Locate every leukocyte (white blood cell).
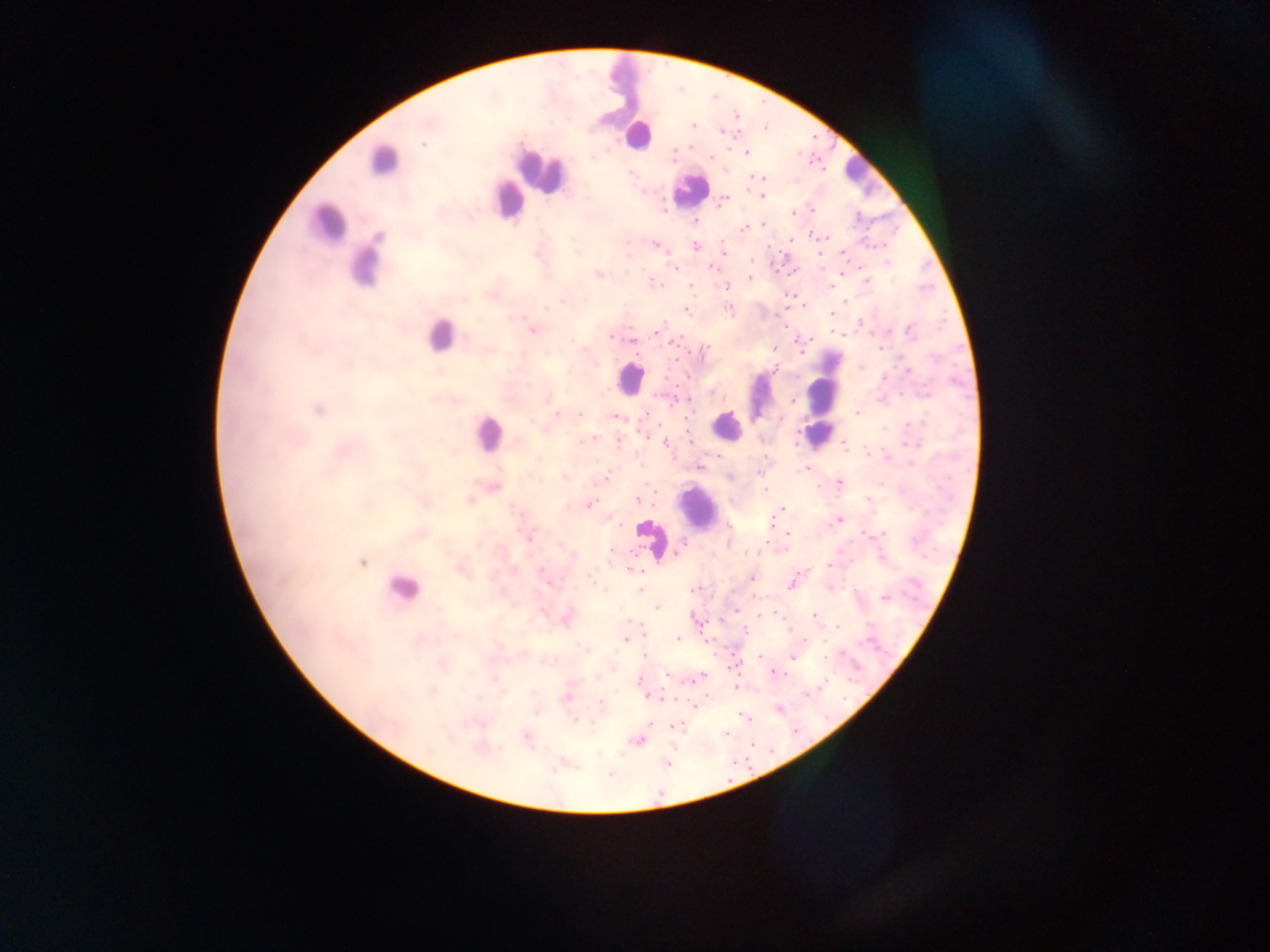
Approximate centers as {x, y} in pixels.
Leukocytes: {624, 86}, {638, 136}, {383, 160}, {541, 170}, {858, 173}, {688, 190}, {506, 199}, {328, 224}, {366, 265}, {438, 335}, {629, 379}, {827, 380}, {759, 397}, {726, 426}, {487, 432}, {816, 433}, {699, 509}, {651, 539}, {401, 588}.

Malaria parasite locations: {692, 126}, {721, 130}, {423, 144}, {747, 152}, {674, 153}, {592, 158}, {710, 158}, {630, 173}, {754, 176}, {762, 178}, {761, 195}, {724, 199}, {812, 211}, {792, 213}, {696, 221}, {763, 225}, {744, 228}, {811, 235}, {790, 240}, {654, 244}, {696, 247}, {576, 253}, {724, 253}, {820, 254}, {752, 262}, {711, 267}, {675, 268}, {599, 275}, {749, 278}, {652, 282}, {867, 282}, {690, 285}, {831, 285}, {726, 286}, {563, 300}, {845, 301}, {546, 308}, {728, 308}, {686, 310}, {831, 314}, {533, 331}, {910, 331}, {657, 332}, {612, 337}, {632, 340}, {674, 342}, {774, 348}, {705, 349}, {774, 370}, {884, 377}, {712, 394}, {925, 396}, {793, 400}, {318, 410}, {558, 413}, {579, 413}, {857, 414}, {614, 417}, {884, 428}, {592, 438}, {619, 441}, {665, 443}, {914, 445}, {845, 447}, {699, 467}, {808, 469}, {564, 476}, {730, 477}, {604, 479}, {839, 484}, {765, 490}, {469, 500}, {636, 500}, {868, 500}, {592, 503}, {782, 508}, {779, 510}, {610, 518}, {839, 521}, {770, 522}, {787, 534}, {884, 534}, {530, 538}, {681, 546}, {611, 554}, {362, 562}, {828, 565}, {542, 570}, {637, 572}, {752, 577}, {593, 582}, {791, 583}, {640, 589}, {695, 589}, {884, 597}, {656, 609}, {735, 611}, {542, 612}, {815, 616}, {838, 627}, {745, 630}, {678, 638}, {806, 639}, {625, 640}, {584, 649}, {645, 654}, {760, 657}, {792, 658}, {776, 673}, {667, 675}, {702, 675}, {640, 681}, {735, 687}, {648, 696}, {566, 698}, {601, 703}, {695, 706}, {743, 716}, {574, 720}, {650, 723}, {677, 727}, {726, 734}, {638, 740}, {609, 775}. Thick blood smear. Collected in Ghana. Mobile-phone photograph taken through the microscope. Image is 1270×952 pixels. Single field of view.